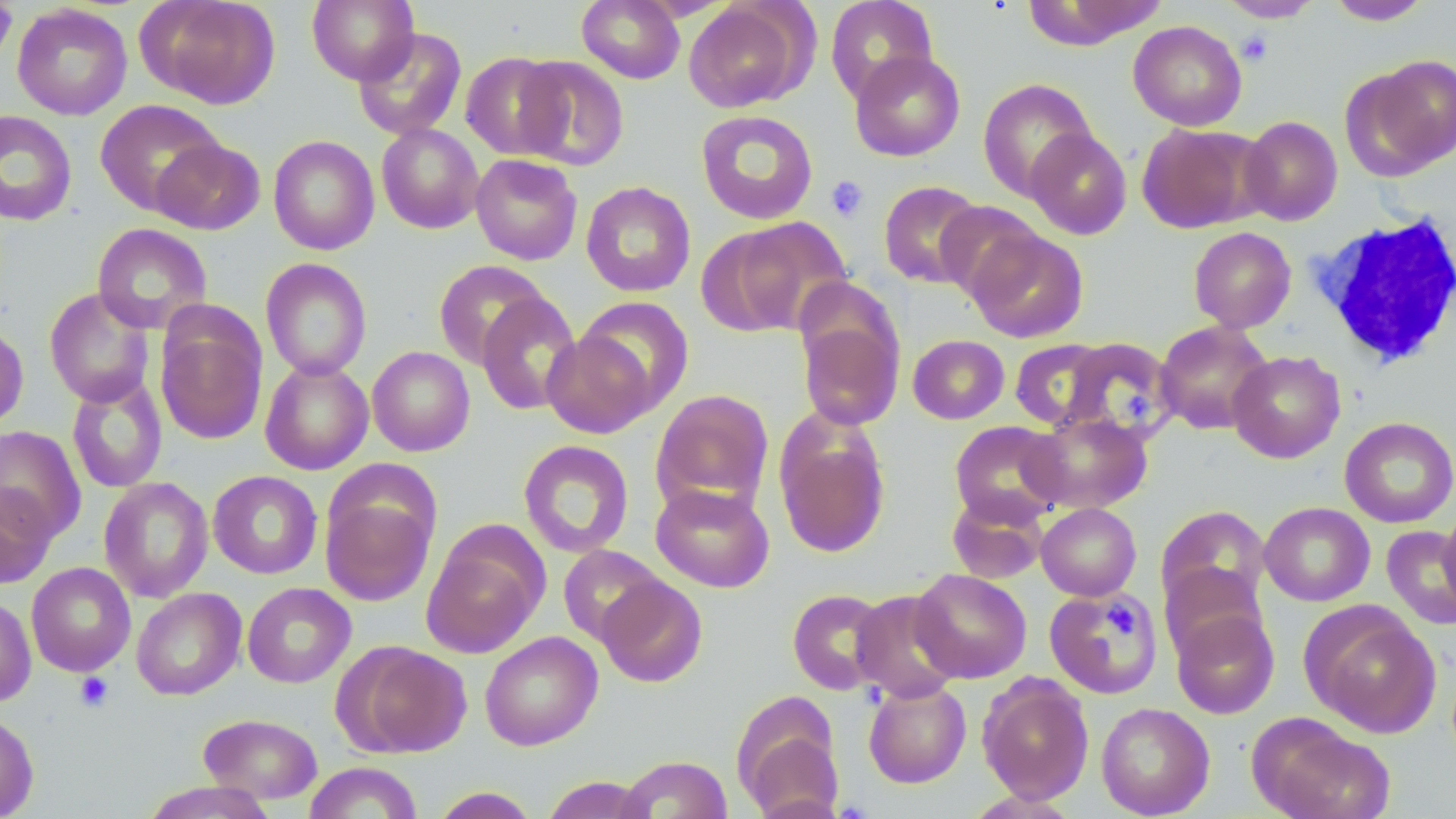
Summary:
  - Coordinate format: approximate bounding boxes as [x1, y1, x2, y2] in pixels
  - White blood cell locations: [1308, 211, 1456, 370]
  - Platelet locations: [1236, 30, 1274, 66], [825, 176, 869, 222], [1122, 388, 1154, 425], [1106, 601, 1136, 640], [75, 672, 113, 711]
  - Uninfected red blood cell locations: [0, 0, 17, 67], [138, 0, 282, 109], [306, 0, 419, 85], [577, 0, 685, 84], [824, 0, 940, 104], [1021, 0, 1166, 49], [1218, 0, 1324, 23], [1325, 0, 1434, 25], [683, 2, 809, 112], [11, 4, 133, 120], [1128, 20, 1247, 131], [353, 27, 467, 140], [849, 50, 966, 161], [460, 51, 570, 160], [514, 55, 630, 171], [1346, 56, 1455, 179], [976, 77, 1097, 201], [94, 99, 225, 216], [695, 109, 819, 225], [0, 110, 77, 226], [1239, 115, 1343, 225], [375, 123, 484, 234], [1136, 123, 1265, 233], [1024, 128, 1132, 240], [268, 135, 379, 255], [151, 138, 265, 235], [471, 154, 583, 265], [580, 180, 696, 297], [878, 180, 986, 289], [934, 200, 1046, 301], [720, 217, 854, 334], [92, 222, 212, 333], [1188, 226, 1297, 333], [966, 227, 1089, 343], [260, 257, 373, 380], [433, 259, 550, 369], [43, 288, 156, 408], [476, 293, 582, 416], [575, 296, 695, 416], [155, 310, 267, 445], [797, 313, 904, 431], [1154, 320, 1274, 435], [0, 323, 29, 432], [542, 331, 656, 438], [908, 334, 1009, 424], [1009, 338, 1110, 429], [1059, 339, 1174, 441], [367, 346, 475, 456], [1228, 350, 1346, 463], [260, 359, 375, 475], [66, 374, 168, 494], [651, 389, 774, 514], [774, 410, 892, 560], [1025, 411, 1153, 514], [1339, 416, 1456, 528], [949, 420, 1068, 527], [0, 425, 86, 544], [518, 440, 634, 558], [208, 471, 323, 579], [98, 476, 214, 602], [651, 482, 775, 592], [0, 484, 57, 589], [321, 490, 437, 607], [947, 491, 1049, 585], [1259, 501, 1375, 606], [1036, 502, 1141, 601], [1155, 505, 1271, 618], [1437, 506, 1456, 612], [1381, 525, 1456, 631], [421, 526, 547, 658], [558, 544, 666, 646], [26, 562, 136, 676], [1160, 562, 1266, 662], [910, 568, 1032, 683], [596, 575, 708, 688], [242, 582, 355, 688], [1043, 586, 1163, 699], [132, 588, 246, 700], [787, 588, 891, 695], [851, 589, 964, 703], [0, 595, 36, 707], [1301, 602, 1441, 738], [1171, 607, 1279, 719], [480, 631, 603, 751], [341, 641, 472, 758], [977, 674, 1095, 804], [863, 680, 972, 788], [731, 693, 845, 819], [1096, 702, 1215, 818], [0, 711, 39, 819], [199, 713, 323, 804], [1249, 715, 1395, 819], [617, 755, 733, 818], [303, 762, 423, 819], [540, 775, 654, 818], [140, 781, 279, 818], [429, 786, 540, 818]
  - Slide-level diagnosis: no evidence of blood parasites
  - Modality: light microscopy
  - Stain: May-Grünwald-Giemsa
  - Magnification: 1000x
  - Image size: 1456×819 pixels
  - Field of view: one of a larger specimen
  - Preparation: thin blood film